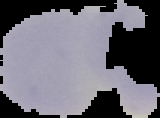
result = negative for malaria parasites
image size = 160×118 pixels
preparation = thin blood film
image type = segmented cell region with the area outside set to black